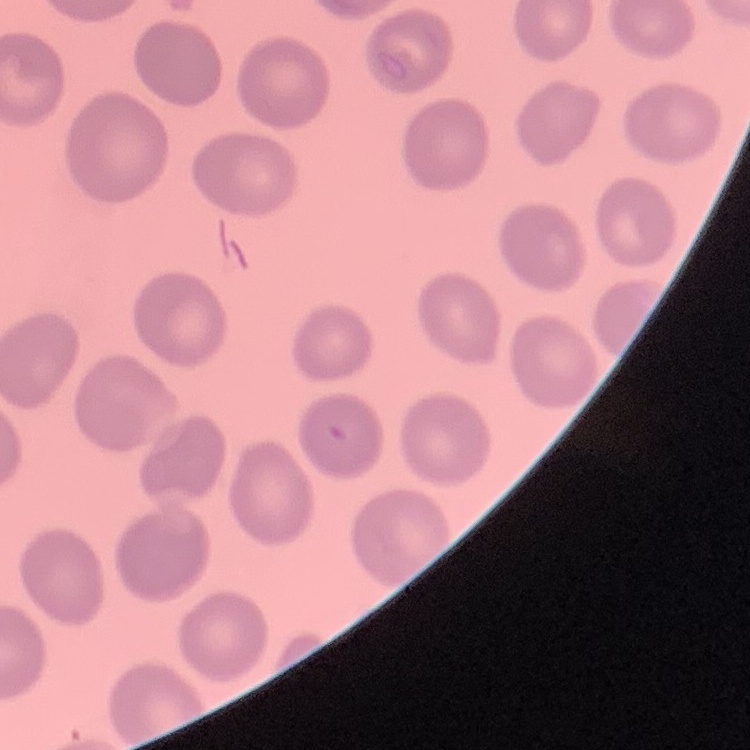

The red blood cells exhibit no rouleaux formation. Square crop of a larger photomicrograph. Thin peripheral smear. Field's or Giemsa stain.